Assess this cell for malaria.
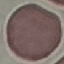

Uninfected.

Photographed with a smartphone camera at the microscope eyepiece. Cell patch, automatically extracted from a larger field of view and resized to 64 × 64 pixels. Thin blood smear. Giemsa stain.